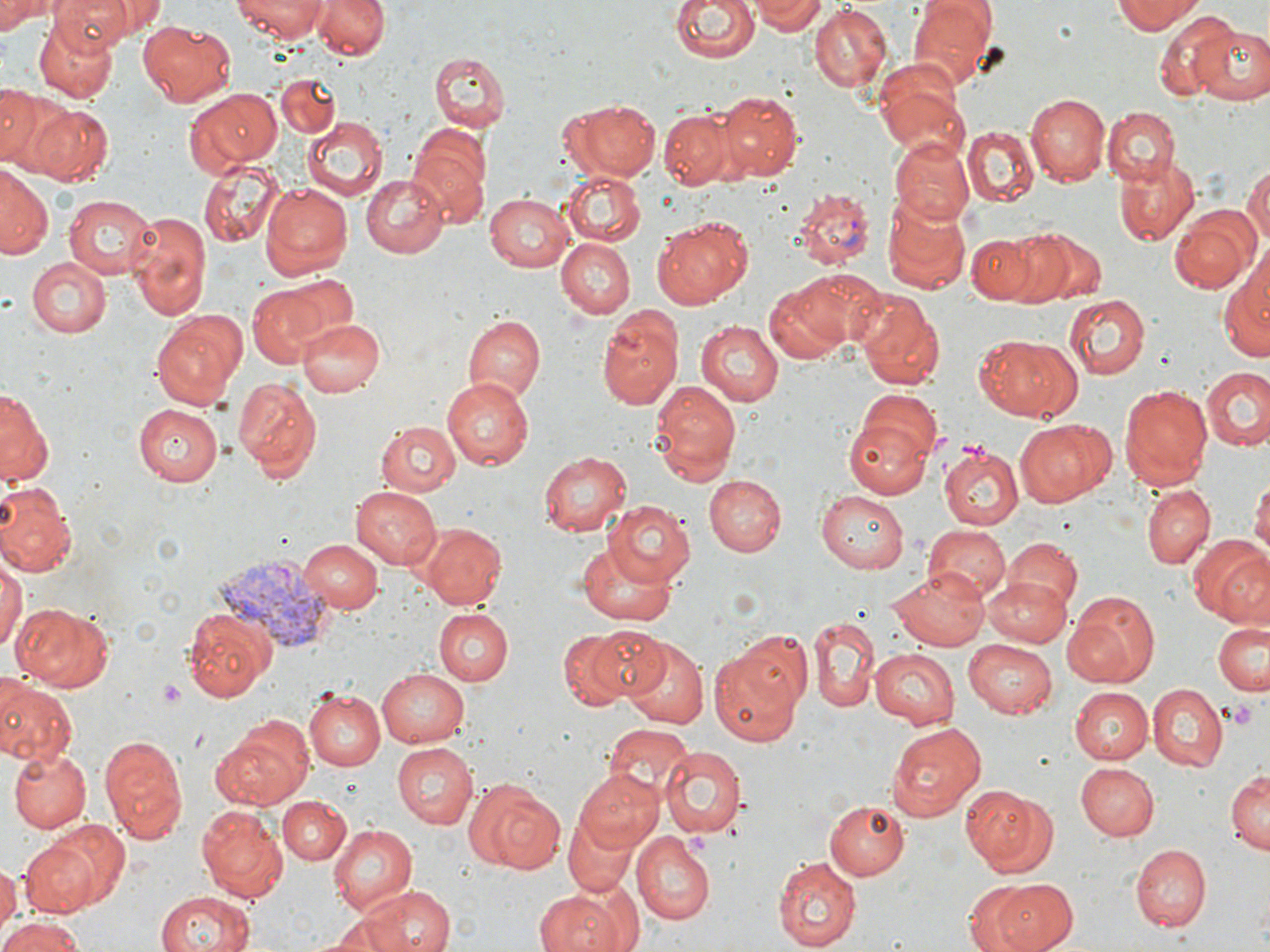 Approximate bounding boxes as [x1, y1, x2, y2] in pixels. Plasmodium vivax-infected red blood cell locations: [791, 187, 874, 267], [209, 556, 341, 649]. Platelet locations: [159, 679, 186, 710], [1226, 698, 1259, 732], [683, 829, 710, 856]. Uninfected red blood cell locations: [0, 0, 55, 35], [49, 0, 143, 50], [233, 0, 329, 39], [312, 0, 392, 61], [671, 0, 758, 65], [755, 0, 824, 34], [907, 0, 998, 84], [1113, 0, 1200, 34], [808, 4, 891, 91], [1156, 13, 1242, 101], [33, 17, 118, 103], [137, 20, 236, 106], [1193, 23, 1270, 107], [429, 52, 510, 133], [875, 60, 965, 151], [276, 73, 338, 140], [1, 83, 45, 167], [186, 88, 282, 175], [714, 90, 802, 180], [1027, 91, 1109, 185], [566, 99, 660, 180], [25, 102, 113, 185], [1103, 107, 1177, 185], [659, 108, 738, 189], [304, 117, 386, 200], [409, 126, 491, 227], [964, 126, 1037, 205], [889, 138, 973, 224], [1114, 156, 1198, 243], [200, 161, 283, 245], [1240, 161, 1269, 250], [0, 167, 50, 260], [563, 172, 646, 245], [361, 174, 448, 258], [262, 183, 353, 280], [880, 190, 974, 294], [485, 191, 575, 273], [63, 195, 153, 280], [127, 208, 212, 322], [1168, 208, 1261, 296], [650, 218, 750, 308], [1008, 226, 1099, 308], [968, 229, 1058, 308], [555, 236, 635, 319], [1221, 255, 1270, 366], [26, 257, 112, 336], [791, 268, 887, 349], [265, 274, 359, 352], [764, 283, 850, 365], [247, 285, 329, 366], [857, 292, 946, 391], [1065, 295, 1150, 380], [597, 310, 684, 409], [150, 311, 248, 410], [462, 313, 544, 405], [295, 315, 384, 397], [695, 318, 783, 406], [976, 334, 1081, 421], [1201, 367, 1270, 451], [232, 375, 322, 483], [441, 375, 534, 468], [648, 380, 741, 486], [1116, 382, 1213, 491], [859, 387, 942, 460], [0, 389, 49, 485], [844, 402, 936, 502], [133, 404, 223, 485], [376, 419, 460, 497], [1016, 419, 1116, 508], [939, 443, 1023, 530], [537, 450, 632, 537], [705, 474, 785, 555], [1251, 475, 1270, 563], [0, 480, 76, 578], [352, 484, 441, 569], [1141, 485, 1214, 569], [815, 490, 907, 572], [606, 499, 695, 585], [419, 523, 507, 609], [924, 525, 1011, 604], [1187, 535, 1270, 625], [299, 538, 382, 613], [1001, 538, 1082, 616], [577, 540, 676, 627], [0, 558, 23, 655], [888, 569, 992, 650], [985, 576, 1072, 646], [1065, 590, 1160, 687], [13, 603, 117, 692], [180, 605, 274, 702], [433, 607, 512, 686], [809, 616, 878, 712], [1213, 619, 1270, 697], [586, 625, 670, 699], [553, 630, 642, 710], [620, 639, 709, 729], [963, 639, 1058, 717], [708, 643, 808, 746], [869, 650, 961, 727], [376, 668, 469, 747], [0, 680, 76, 770], [1147, 685, 1226, 771], [1071, 686, 1154, 764], [302, 688, 386, 771], [212, 713, 314, 810], [887, 722, 985, 819], [603, 723, 693, 801], [97, 733, 188, 845], [391, 743, 477, 828], [660, 747, 747, 840], [9, 748, 92, 834], [1075, 763, 1159, 840], [1226, 770, 1269, 852], [575, 772, 665, 850], [461, 778, 566, 875], [959, 784, 1057, 876], [277, 797, 349, 864], [824, 800, 907, 880], [194, 803, 288, 904], [561, 815, 640, 897], [43, 820, 130, 910], [328, 822, 418, 915], [631, 834, 715, 925], [21, 836, 102, 913], [1131, 844, 1208, 931], [772, 852, 861, 951], [15, 857, 92, 948], [0, 860, 19, 941], [990, 879, 1078, 952], [964, 881, 1042, 951], [359, 883, 457, 952], [532, 888, 633, 952], [155, 890, 257, 952], [328, 910, 413, 951], [0, 914, 89, 952]. Slide-level diagnosis: Plasmodium vivax. 1000x magnification. Thin blood smear. One field of a larger specimen. May-Grünwald-Giemsa-stained preparation. Image is 1270×952 pixels. Optical microscopy.